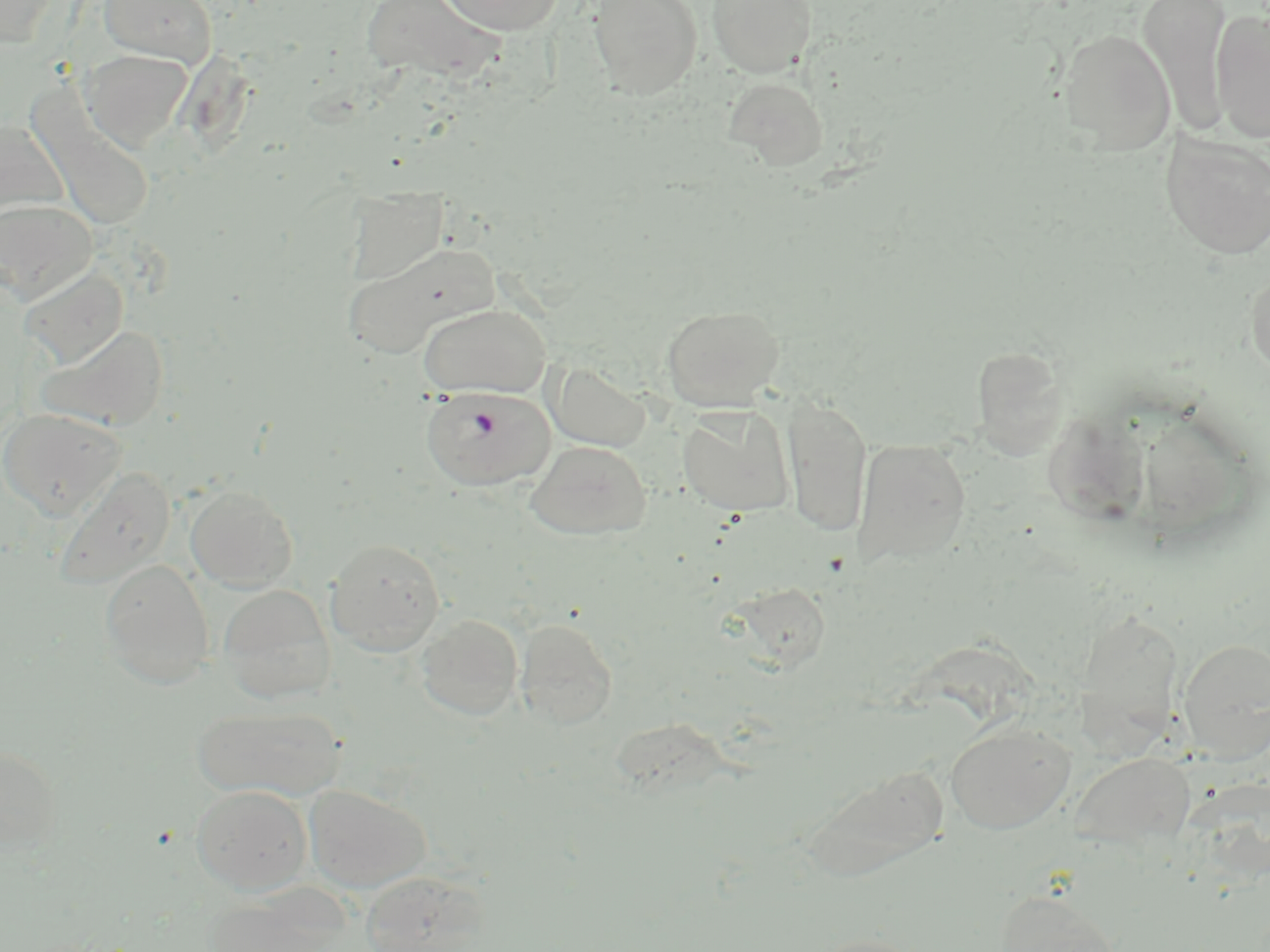

Approximate bounding boxes as [x1, y1, x2, y2] in pixels. Uninfected red blood cell locations: [1, 0, 62, 49], [99, 0, 218, 68], [361, 0, 506, 83], [438, 0, 566, 34], [588, 0, 702, 99], [706, 0, 816, 77], [1139, 0, 1232, 134], [1211, 7, 1270, 145], [1058, 27, 1176, 154], [81, 49, 194, 153], [724, 75, 829, 170], [25, 87, 158, 233], [0, 119, 70, 225], [1160, 133, 1270, 259], [345, 185, 448, 284], [0, 198, 96, 304], [343, 241, 500, 359], [19, 265, 129, 369], [1246, 268, 1270, 381], [418, 303, 552, 398], [661, 304, 784, 411], [36, 323, 169, 430], [972, 344, 1068, 459], [548, 362, 651, 453], [782, 393, 873, 538], [678, 406, 794, 517], [0, 408, 125, 520], [853, 437, 971, 566], [526, 440, 652, 540], [55, 467, 176, 588], [184, 485, 298, 591], [326, 538, 446, 655], [100, 559, 215, 689], [731, 582, 833, 673], [218, 584, 335, 704], [1081, 606, 1183, 746], [416, 613, 523, 721], [515, 616, 618, 729], [1178, 638, 1270, 760], [192, 704, 345, 801], [945, 721, 1074, 834], [0, 744, 63, 854], [1072, 750, 1196, 850], [800, 761, 952, 881], [304, 784, 430, 894], [190, 785, 312, 894], [360, 871, 486, 952], [995, 888, 1123, 952], [204, 891, 338, 952], [809, 932, 927, 952]. Plasmodium falciparum-infected red blood cell locations: [421, 385, 554, 491]. Slide-level diagnosis: Plasmodium falciparum. Light microscopy. Thin blood smear. Single field of view. Image is 1270×952 pixels. May-Grünwald-Giemsa stain. Captured at 1000x magnification.